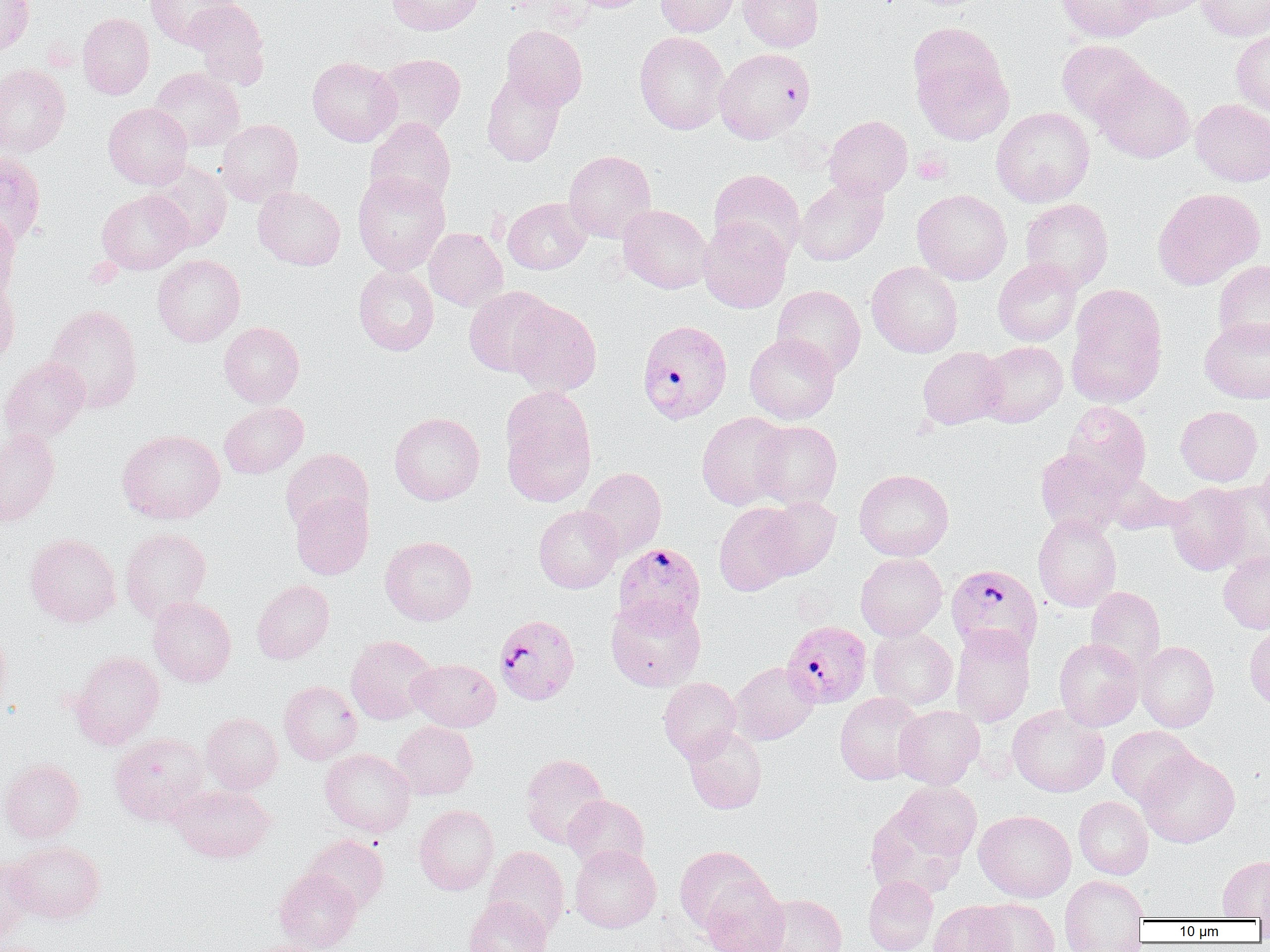

slide-level diagnosis = Plasmodium falciparum
preparation = thin blood smear
field of view = one of a larger specimen
modality = optical microscopy
Plasmodium falciparum-infected red blood cell locations = approximate bounding boxes as [x1, y1, x2, y2] in pixels: [639, 322, 735, 427], [613, 542, 706, 632], [943, 562, 1040, 655], [494, 613, 580, 705], [782, 621, 872, 708]
image size = 1270×952 pixels
uninfected red blood cell locations = approximate bounding boxes as [x1, y1, x2, y2] in pixels: [0, 0, 34, 57], [145, 0, 239, 48], [185, 0, 269, 88], [387, 0, 484, 35], [569, 0, 650, 12], [655, 0, 740, 36], [738, 0, 823, 51], [1057, 0, 1157, 43], [1119, 0, 1210, 22], [1196, 0, 1270, 41], [78, 12, 154, 100], [907, 23, 1013, 144], [501, 24, 587, 110], [1231, 30, 1270, 121], [634, 31, 728, 134], [1057, 40, 1152, 124], [714, 47, 815, 144], [373, 54, 465, 137], [307, 56, 402, 146], [0, 64, 71, 157], [149, 67, 245, 151], [1092, 67, 1194, 163], [481, 70, 567, 166], [1191, 98, 1270, 186], [104, 103, 193, 189], [991, 107, 1095, 207], [824, 115, 913, 200], [365, 117, 456, 209], [215, 119, 303, 207], [564, 150, 656, 242], [0, 152, 46, 248], [143, 159, 232, 252], [708, 169, 805, 261], [352, 170, 451, 275], [794, 176, 889, 266], [253, 186, 345, 270], [1152, 187, 1264, 290], [912, 189, 1012, 285], [97, 190, 191, 274], [503, 197, 591, 275], [1020, 198, 1114, 291], [618, 204, 712, 293], [0, 212, 20, 301], [698, 216, 792, 313], [424, 227, 507, 311], [153, 255, 245, 347], [993, 257, 1082, 346], [1213, 259, 1270, 351], [866, 261, 963, 358], [354, 265, 439, 356], [0, 280, 20, 368], [772, 285, 865, 379], [464, 286, 555, 377], [1066, 286, 1167, 408], [507, 298, 602, 396], [44, 303, 143, 413], [1200, 317, 1270, 403], [219, 321, 304, 407], [744, 333, 840, 424], [977, 340, 1068, 427], [917, 347, 1007, 429], [0, 357, 90, 445], [499, 385, 598, 508], [1062, 401, 1151, 491], [219, 402, 308, 478], [1175, 405, 1262, 486], [696, 411, 791, 510], [389, 412, 485, 505], [751, 420, 842, 509], [117, 429, 225, 524], [0, 430, 59, 527], [280, 448, 373, 534], [1035, 448, 1128, 536], [1256, 453, 1270, 533], [580, 467, 666, 559], [854, 469, 954, 561], [1102, 473, 1184, 535], [1166, 482, 1253, 575], [1212, 483, 1270, 571], [291, 492, 374, 579], [759, 497, 841, 579], [714, 502, 802, 596], [534, 505, 622, 593], [1033, 513, 1121, 612], [120, 528, 211, 622], [25, 533, 121, 627], [380, 535, 477, 625], [1218, 549, 1270, 633], [855, 553, 947, 640], [252, 580, 334, 664], [1085, 586, 1166, 674], [148, 596, 236, 686], [606, 597, 706, 691], [1244, 622, 1270, 710], [0, 625, 12, 716], [868, 626, 958, 709], [950, 626, 1035, 727], [345, 635, 438, 725], [1054, 637, 1144, 731], [1136, 641, 1218, 732], [69, 650, 165, 748], [408, 658, 501, 731], [729, 661, 819, 745], [658, 677, 741, 762], [280, 681, 361, 763], [835, 692, 926, 784], [1008, 704, 1109, 797], [895, 705, 984, 788], [201, 713, 282, 793], [392, 721, 478, 799], [683, 725, 767, 814], [1107, 726, 1197, 808], [110, 733, 210, 826], [321, 748, 416, 837], [1138, 749, 1240, 848], [520, 753, 609, 848], [0, 758, 84, 843], [893, 781, 981, 860], [169, 784, 274, 862], [563, 795, 649, 872], [1073, 796, 1153, 879], [414, 804, 499, 895], [865, 807, 966, 900], [974, 809, 1076, 902], [303, 834, 389, 912], [6, 840, 105, 923], [569, 844, 661, 933], [484, 846, 569, 937], [674, 846, 770, 934], [0, 855, 37, 943], [1218, 856, 1270, 919], [275, 868, 362, 952], [863, 875, 938, 952], [1059, 875, 1148, 951], [700, 877, 789, 952], [756, 893, 847, 952], [463, 897, 551, 952], [972, 898, 1059, 952], [929, 900, 1018, 952], [241, 939, 329, 952], [0, 941, 50, 952]
magnification = 1000x
platelet locations = approximate bounding boxes as [x1, y1, x2, y2] in pixels: [912, 150, 951, 184], [85, 258, 123, 287]